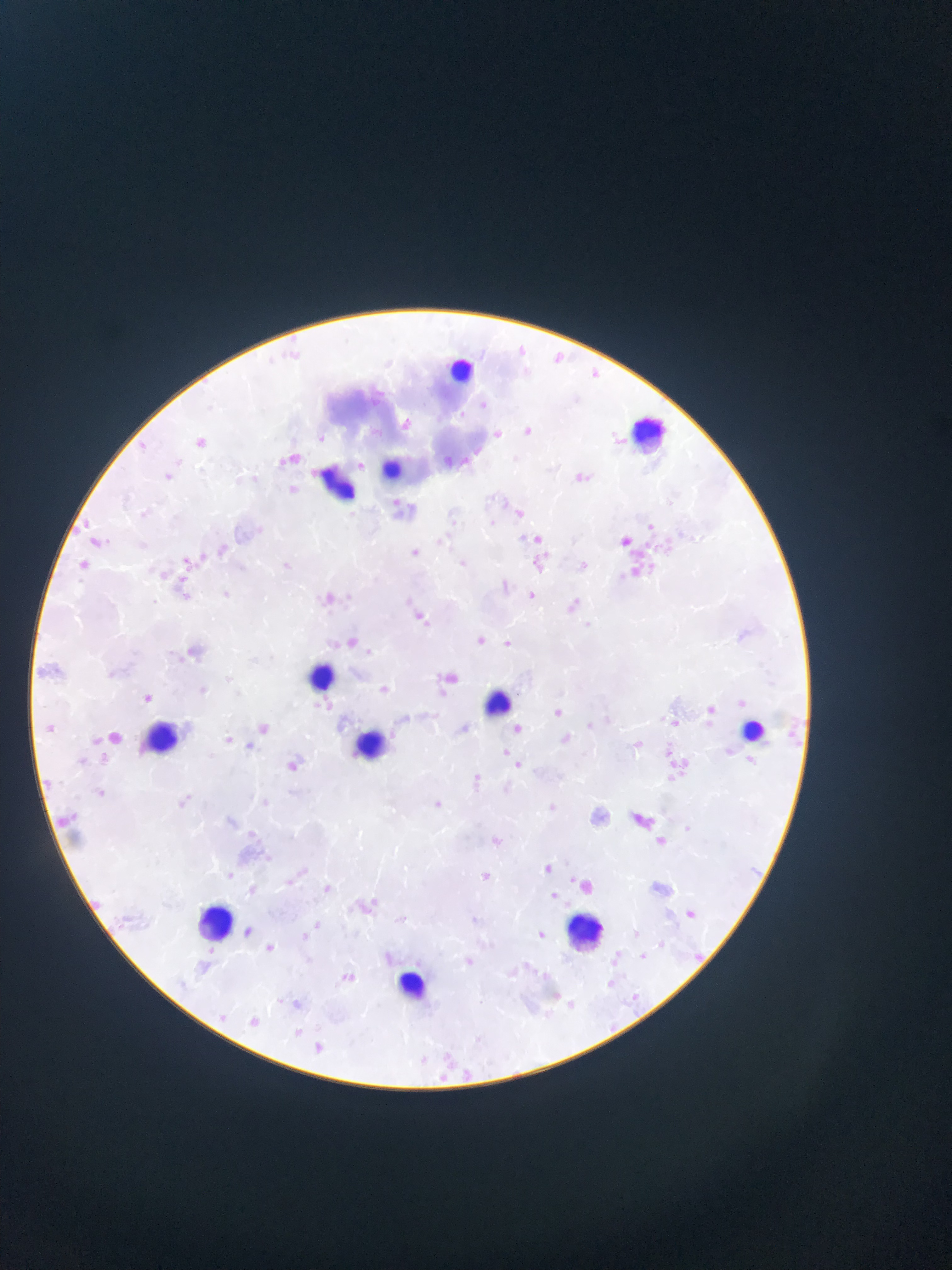
Approximate bounding boxes as {left, top, right, bottom} in pixels. Leukocyte locations: {443, 347, 473, 398}, {628, 412, 664, 458}, {368, 452, 404, 493}, {304, 459, 356, 502}, {309, 656, 339, 707}, {478, 682, 512, 720}, {136, 715, 197, 755}, {742, 715, 774, 745}, {355, 722, 387, 759}, {190, 902, 245, 942}, {551, 911, 605, 955}, {376, 960, 444, 1013}. Malaria parasite locations: {517, 344, 536, 367}, {553, 349, 571, 361}, {584, 363, 599, 378}, {367, 383, 391, 406}, {399, 416, 425, 438}, {521, 422, 534, 438}, {365, 425, 393, 443}, {490, 426, 509, 450}, {609, 430, 628, 449}, {194, 431, 219, 463}, {289, 450, 306, 464}, {442, 455, 461, 472}, {160, 469, 182, 488}, {575, 473, 602, 492}, {288, 483, 303, 501}, {508, 507, 527, 522}, {532, 533, 543, 543}, {614, 534, 634, 547}, {85, 536, 105, 554}, {197, 549, 208, 566}, {408, 549, 421, 557}, {166, 551, 194, 573}, {172, 582, 192, 595}, {320, 584, 339, 613}, {522, 589, 548, 602}, {344, 590, 361, 609}, {410, 598, 431, 616}, {420, 610, 439, 632}, {340, 630, 359, 645}, {474, 635, 484, 645}, {498, 637, 511, 646}, {437, 681, 445, 697}, {369, 682, 394, 698}, {723, 692, 749, 709}, {143, 694, 153, 703}, {554, 708, 563, 717}, {699, 708, 721, 732}, {663, 711, 682, 728}, {514, 723, 523, 732}, {254, 724, 276, 739}, {560, 730, 596, 752}, {631, 733, 645, 747}, {238, 742, 255, 751}, {493, 742, 524, 770}, {292, 756, 309, 780}, {667, 757, 693, 772}, {463, 770, 491, 791}, {545, 799, 572, 829}, {625, 811, 662, 832}, {475, 832, 512, 853}, {749, 865, 768, 878}, {545, 866, 554, 873}, {286, 870, 305, 895}, {483, 871, 493, 880}, {317, 880, 330, 895}, {353, 900, 377, 923}, {681, 909, 699, 924}, {397, 917, 407, 925}, {312, 920, 338, 940}, {533, 925, 555, 944}, {302, 932, 311, 945}, {264, 940, 277, 956}, {632, 947, 652, 960}, {695, 949, 714, 965}, {336, 963, 366, 991}, {605, 975, 633, 997}, {630, 988, 642, 1001}, {289, 994, 319, 1017}, {249, 1014, 281, 1037}, {610, 1022, 626, 1042}, {288, 1024, 313, 1041}, {307, 1041, 333, 1054}, {428, 1053, 450, 1082}, {457, 1055, 487, 1085}. Collected in Ghana. Thin blood smear. Single field of view. Image is 952×1270 pixels. Photographed through a microscope with a mobile-phone camera.